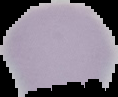
From a thin blood film. Image is 118×97 pixels. Cell region segmented out of the field of view; the surrounding area is masked to black. Result: Plasmodium parasites detected.